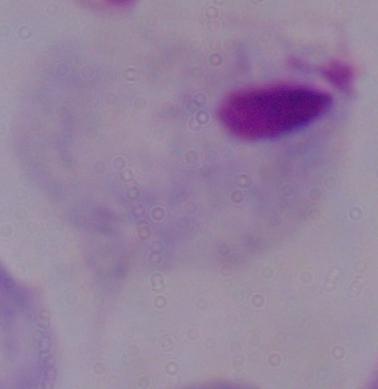 Micrograph. Captured at 1000x magnification. A trichomonad is shown.